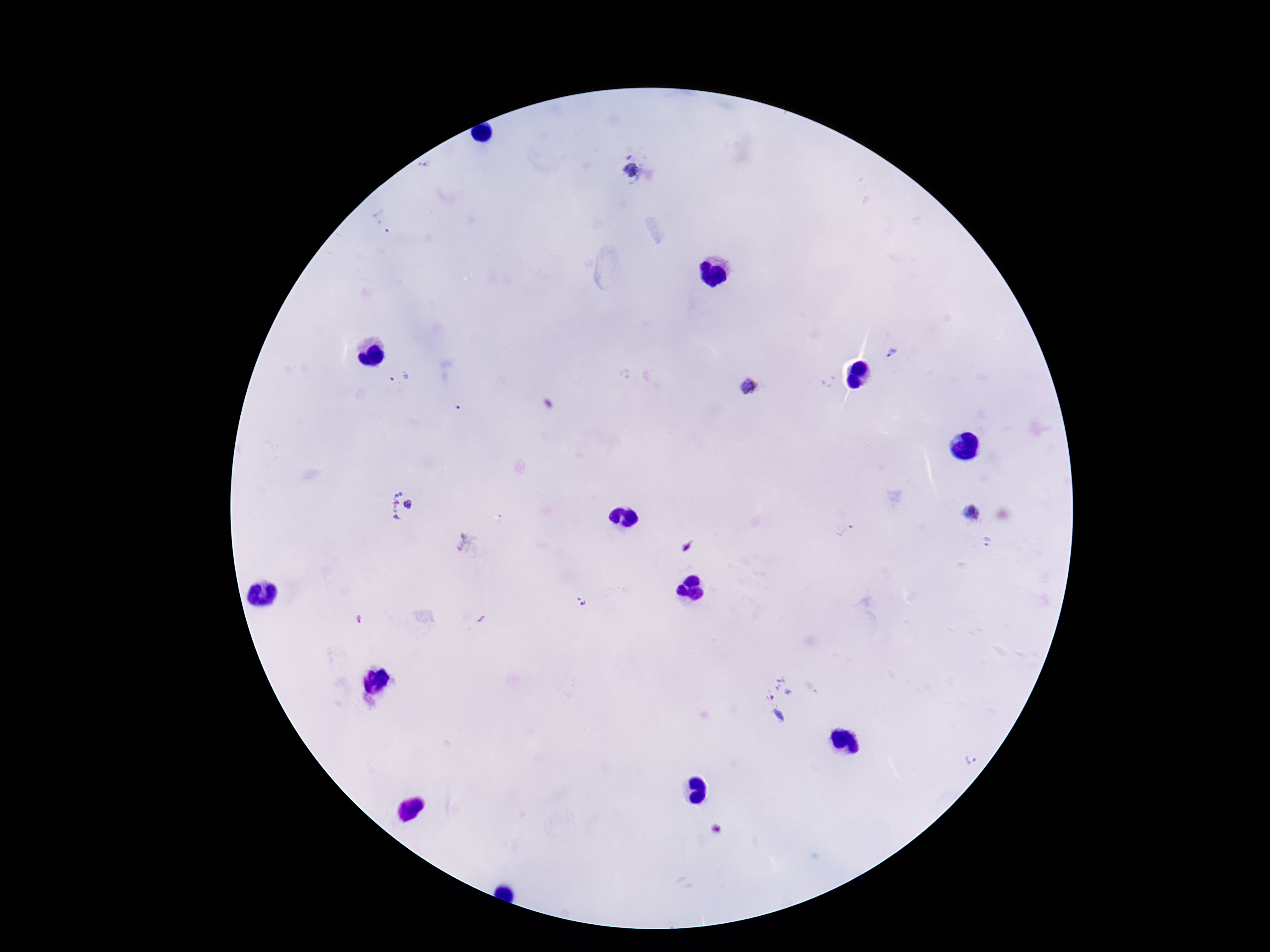
Approximate object centers, in pixels from the top-left corner. Plasmodium parasite locations: (x=427, y=163), (x=632, y=173), (x=383, y=223), (x=894, y=353), (x=626, y=376), (x=401, y=378), (x=751, y=387), (x=409, y=505), (x=397, y=506), (x=970, y=513), (x=845, y=531), (x=986, y=543), (x=469, y=545), (x=687, y=545), (x=581, y=602), (x=358, y=620), (x=482, y=620), (x=780, y=699), (x=971, y=760), (x=717, y=828). Patient malaria status: infected. 100x magnification. One field from this slide. Thick blood smear. Photographed through the microscope eyepiece with a smartphone camera. Giemsa stain. Image is 1270×952 pixels.